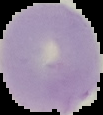

image_type: cell region segmented out of the field of view; surrounding area masked to black
image_size: 103×115 pixels
preparation: thin blood film
malaria_status: uninfected